Assess this cell for malaria.
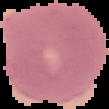
It is uninfected.

Image is 109×109 pixels. From a thin blood film. The area outside the segmented cell region is set to black.